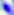

magnification = 400x
identification = Toxoplasma gondii
modality = photomicrograph